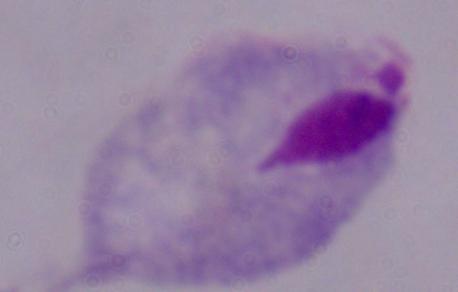

Summary:
  - Magnification: 1000x
  - Modality: photomicrograph
  - Identification: trichomonad